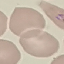
Summary:
  - Malaria status: parasitized
  - Stain: Giemsa
  - Capture: smartphone through the microscope eyepiece
  - Image type: automatically extracted cell patch, resized to 64 × 64 pixels
  - Preparation: thin smear